Describe the morphology of the red blood cells.
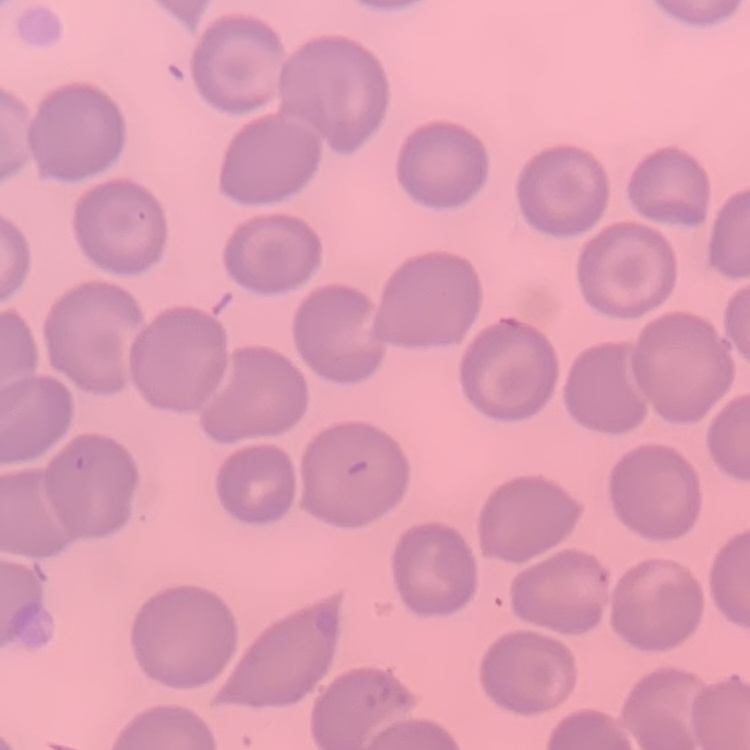
No rouleaux formation.

Stained with either Field's or Giemsa. Thin peripheral smear. Square crop of a larger photomicrograph.